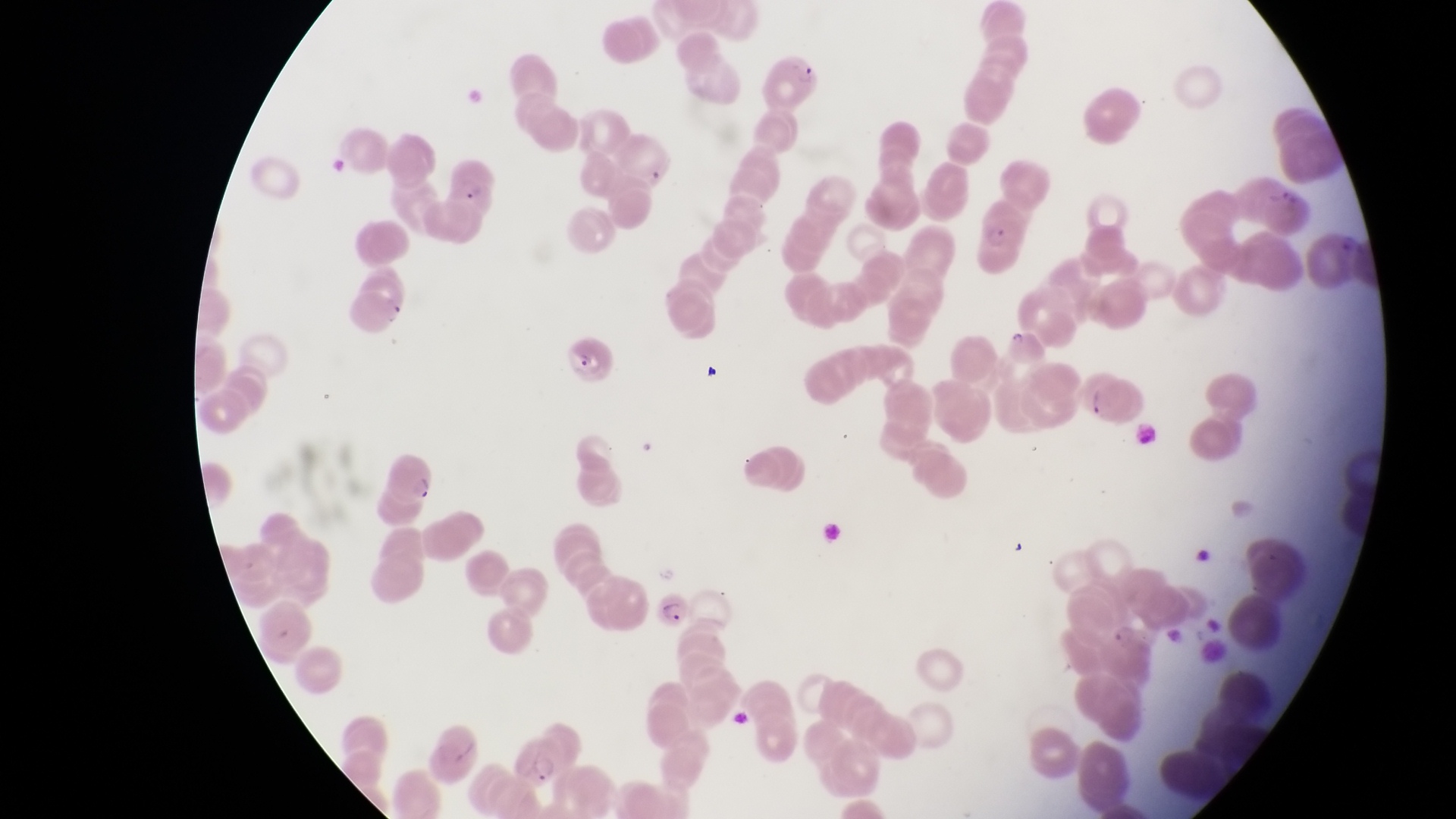

Approximate bounding boxes as [left, top, right, bottom] in pixels. Parasitised red blood cell locations: [446, 155, 498, 211], [977, 215, 1032, 281], [343, 285, 407, 334], [557, 328, 612, 384], [1080, 373, 1143, 425], [377, 447, 436, 510], [647, 591, 696, 630], [502, 733, 576, 792]. Image is 1456×819 pixels. One field of view. Sample from Uganda. Magnification of 1000x. Thin blood film. Captured by a smartphone held over the eyepiece of an Olympus CX-23 microscope.